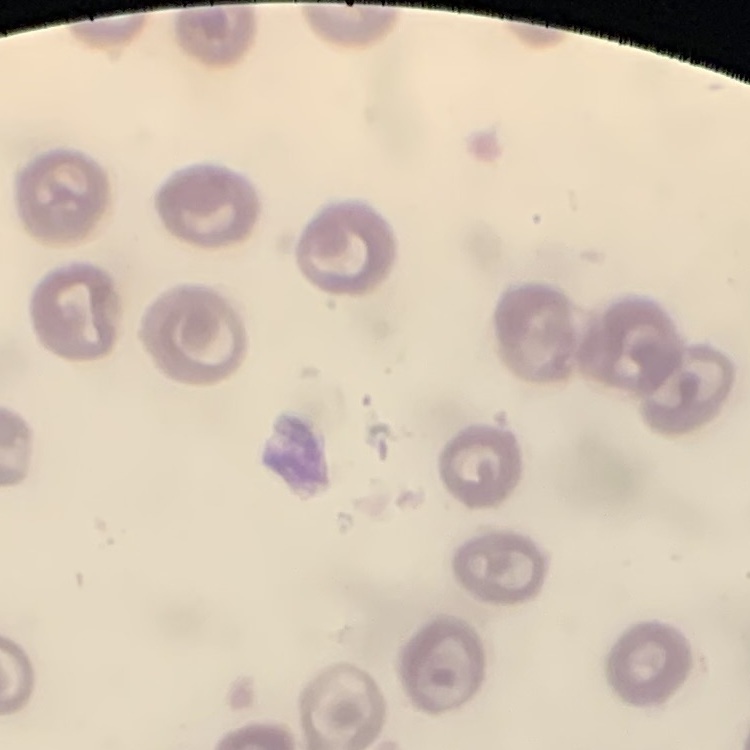

Summary:
  - Erythrocyte morphology: no rouleaux formation
  - Image type: square crop of a larger photomicrograph
  - Preparation: thin blood smear
  - Stain: Field's or Giemsa